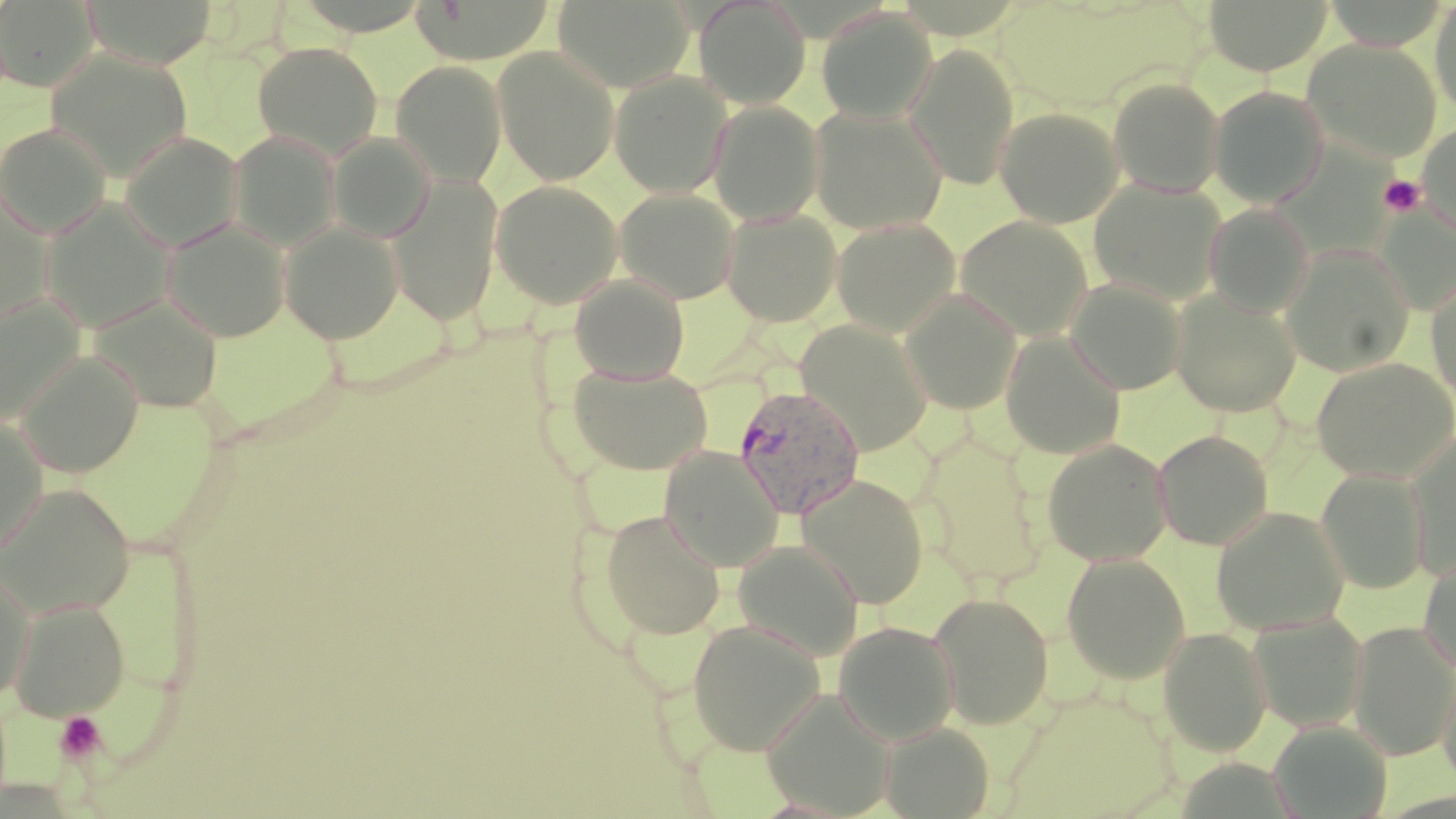
Summary:
  - Coordinate format: approximate bounding boxes as (x1,y1)-(x2,y2) corner pairs in pixels
  - Platelet locations: (1379,175)-(1425,217), (53,711)-(108,765)
  - Plasmodium malariae-infected red blood cell locations: (733,384)-(865,520)
  - Uninfected red blood cell locations: (80,0)-(219,69), (410,0)-(559,64), (553,0)-(694,93), (694,0)-(811,109), (1204,0)-(1332,76), (1430,0)-(1456,118), (0,1)-(99,92), (817,9)-(937,124), (1303,39)-(1442,162), (252,42)-(383,160), (904,44)-(1021,189), (44,48)-(194,182), (493,48)-(620,185), (390,60)-(506,186), (609,70)-(733,198), (1108,78)-(1224,198), (1209,87)-(1328,208), (708,100)-(824,225), (994,106)-(1124,228), (809,107)-(948,235), (0,123)-(112,240), (1417,124)-(1456,234), (226,130)-(343,252), (120,132)-(244,252), (327,132)-(436,243), (387,175)-(503,326), (489,180)-(623,308), (1089,180)-(1226,305), (0,188)-(57,335), (615,188)-(740,304), (40,198)-(176,332), (1205,204)-(1314,317), (721,209)-(843,326), (955,216)-(1095,341), (160,218)-(292,342), (831,218)-(961,337), (279,221)-(404,343), (1281,243)-(1416,377), (1426,271)-(1456,405), (569,274)-(689,384), (1065,277)-(1187,394), (899,288)-(1024,415), (1169,291)-(1300,417), (89,294)-(223,413), (1,296)-(86,423), (796,320)-(934,455), (1000,330)-(1125,459), (15,351)-(144,478), (1310,357)-(1456,483), (567,364)-(714,476), (0,412)-(48,558), (1153,429)-(1274,550), (915,432)-(1049,590), (1406,433)-(1456,580), (1041,439)-(1172,566), (659,446)-(783,571), (1316,468)-(1431,594), (797,473)-(930,609), (1,484)-(134,618), (1211,506)-(1350,636), (598,509)-(727,640), (732,538)-(865,662), (1061,553)-(1190,684), (1418,554)-(1456,674), (1,564)-(35,702), (928,591)-(1055,729), (8,598)-(131,721), (1247,613)-(1369,732), (687,619)-(826,756), (1348,620)-(1456,761), (833,621)-(960,745), (1158,627)-(1272,756), (1439,661)-(1456,793), (760,689)-(897,817), (1006,693)-(1185,816), (1267,720)-(1393,818), (879,722)-(995,818)
  - Slide-level diagnosis: Plasmodium malariae
  - Image size: 1456×819 pixels
  - Stain: May-Grünwald-Giemsa
  - Preparation: thin blood film
  - Modality: optical microscopy
  - Magnification: 1000x
  - Field of view: one of a larger specimen